Assess this cell for malaria.
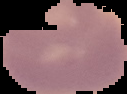

It is uninfected.

From a thin blood smear. Image is 127×94 pixels. Cell region segmented out of the field of view; the surrounding area is masked to black.